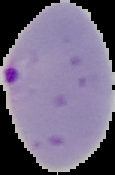
Summary:
  - Malaria status: parasitized
  - Preparation: thin blood film
  - Image type: segmented cell region with the area outside set to black
  - Image size: 115×175 pixels